Comment on the morphology of the erythrocytes.
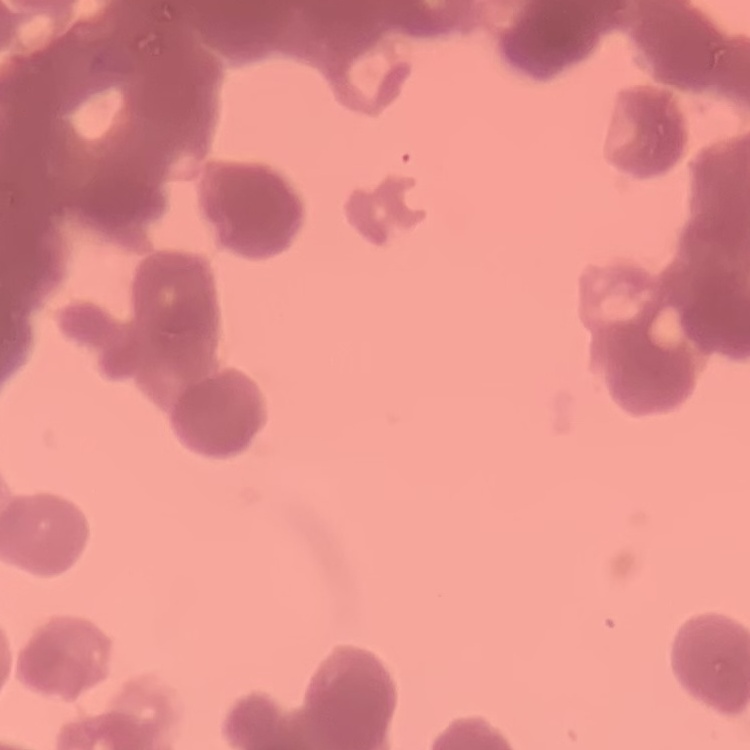

Rouleaux formation.

Summary:
  - Stain: Field's or Giemsa
  - Preparation: thin blood smear
  - Image type: one tile cut from a larger photomicrograph